Name the parasite shown.
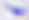
This is Toxoplasma gondii.

modality = micrograph
magnification = 400x